Locate and identify every blood parasite.
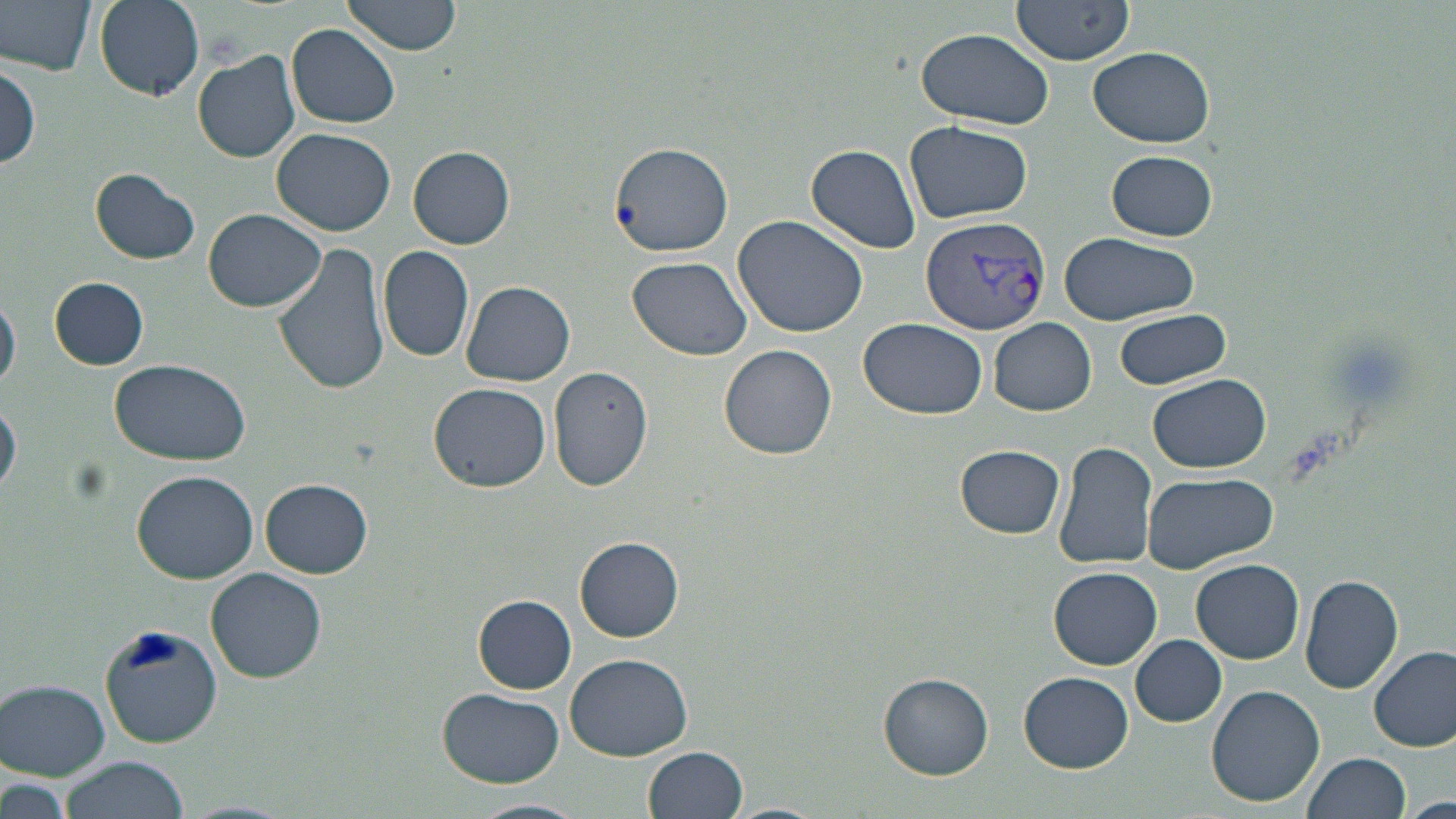

Approximate bounding boxes as [x1, y1, x2, y2] in pixels.
Plasmodium vivax-infected red blood cells: [921, 215, 1051, 336].
No Plasmodium falciparum, Plasmodium ovale, Plasmodium malariae, Babesia divergens, or Trypanosoma brucei observed.

Summary:
  - Uninfected red blood cell locations: [1, 0, 100, 76], [92, 0, 206, 102], [342, 0, 463, 56], [1010, 0, 1136, 65], [287, 26, 402, 128], [914, 27, 1057, 129], [1089, 45, 1215, 147], [193, 50, 300, 162], [1, 64, 42, 173], [905, 120, 1032, 225], [272, 127, 395, 236], [608, 141, 735, 258], [806, 143, 921, 253], [409, 146, 515, 248], [1106, 151, 1218, 241], [90, 169, 200, 266], [203, 208, 326, 313], [732, 213, 869, 338], [1058, 232, 1200, 325], [273, 242, 393, 397], [379, 245, 475, 362], [627, 256, 753, 360], [49, 276, 149, 370], [460, 281, 576, 386], [0, 293, 20, 396], [1113, 308, 1232, 391], [859, 317, 988, 421], [989, 317, 1096, 416], [718, 343, 839, 460], [111, 358, 250, 466], [549, 366, 654, 491], [1148, 374, 1271, 473], [429, 381, 551, 493], [0, 398, 21, 496], [1053, 441, 1159, 572], [956, 444, 1064, 537], [131, 471, 258, 583], [1141, 472, 1278, 574], [262, 479, 372, 577], [575, 537, 684, 641], [1192, 559, 1304, 663], [1050, 566, 1162, 668], [206, 568, 326, 682], [1299, 573, 1404, 694], [473, 594, 576, 693], [101, 622, 224, 746], [1131, 634, 1226, 727], [1370, 644, 1455, 752], [564, 653, 693, 761], [879, 672, 993, 779], [1020, 672, 1132, 772], [2, 679, 111, 778], [1206, 685, 1325, 807], [437, 688, 567, 786], [645, 747, 749, 819], [1304, 752, 1409, 818], [59, 756, 188, 819], [1, 776, 73, 819], [1402, 797, 1456, 819], [471, 798, 591, 819], [717, 803, 829, 819]
  - Slide-level diagnosis: Plasmodium vivax
  - Modality: optical microscopy
  - Field of view: single
  - Stain: May-Grünwald-Giemsa
  - Image size: 1456×819 pixels
  - Magnification: 1000x
  - Preparation: thin blood film